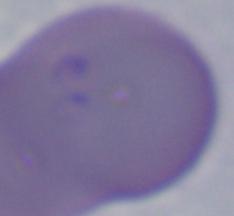

magnification = 1000x
identification = Babesia
modality = photomicrograph